Give the extent of all Plasmodium vivax-infected red blood cells.
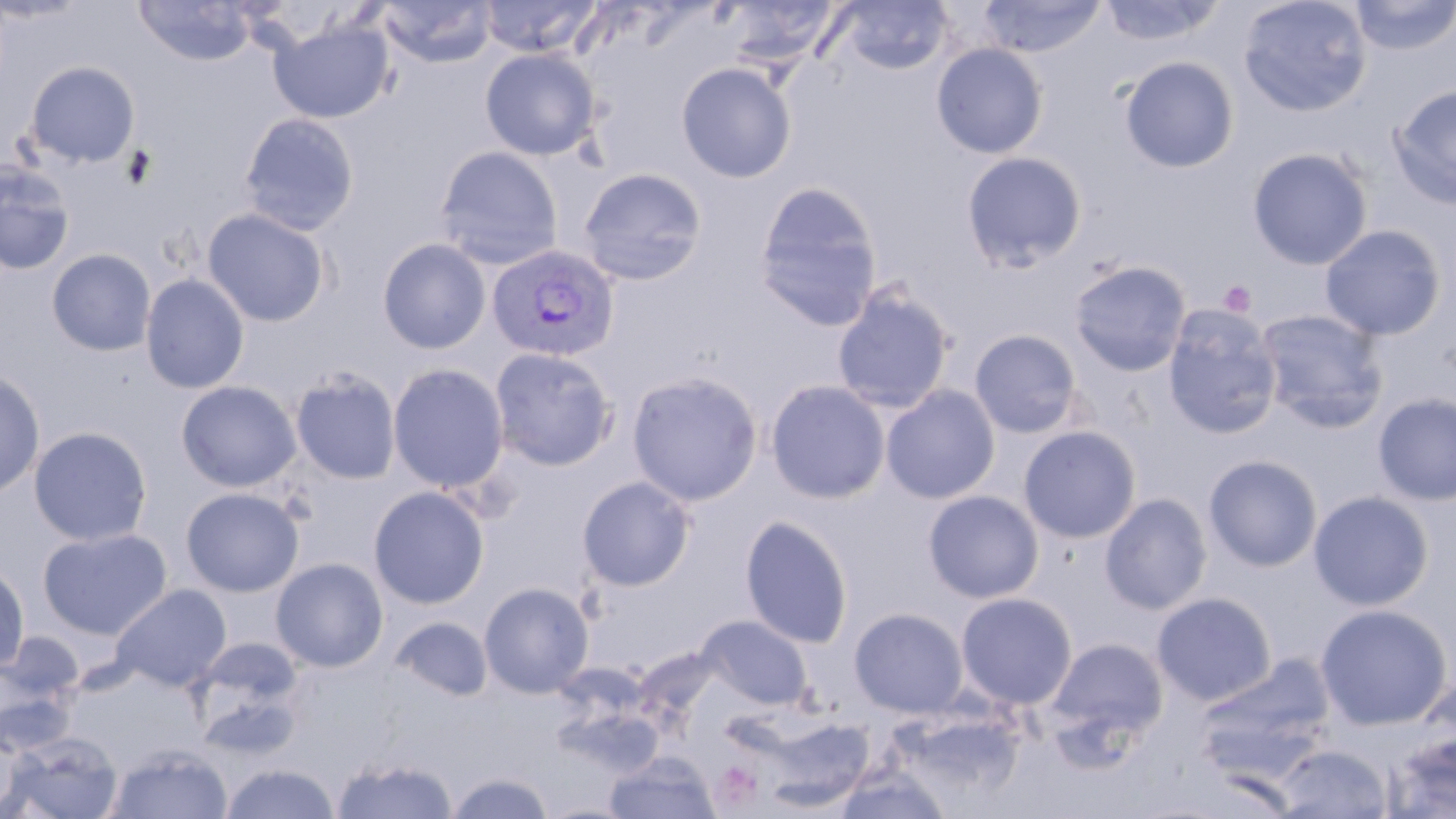

Approximate bounding boxes as [x1, y1, x2, y2] in pixels.
Plasmodium vivax-infected red blood cells: [487, 244, 621, 363].

Platelet locations: [1219, 280, 1256, 317], [713, 763, 761, 808]. Uninfected red blood cell locations: [133, 0, 258, 67], [378, 0, 497, 67], [478, 0, 601, 58], [720, 0, 842, 69], [834, 0, 953, 75], [977, 0, 1107, 58], [1098, 0, 1225, 46], [1238, 0, 1372, 117], [1349, 0, 1456, 55], [270, 20, 394, 123], [932, 43, 1048, 159], [480, 47, 602, 160], [1119, 56, 1239, 173], [24, 61, 140, 168], [676, 62, 796, 182], [1388, 84, 1456, 210], [240, 113, 359, 235], [435, 146, 563, 269], [1247, 147, 1372, 270], [961, 151, 1087, 272], [0, 160, 75, 275], [578, 167, 707, 286], [753, 181, 883, 332], [201, 207, 331, 327], [1319, 224, 1446, 341], [377, 238, 491, 354], [47, 248, 156, 356], [1070, 260, 1191, 377], [139, 273, 250, 394], [831, 285, 955, 413], [1163, 306, 1282, 439], [1255, 309, 1390, 434], [969, 329, 1082, 438], [489, 347, 619, 472], [388, 363, 509, 493], [289, 368, 402, 486], [0, 369, 45, 498], [626, 370, 763, 506], [766, 379, 891, 504], [175, 380, 302, 492], [881, 385, 1000, 504], [1372, 393, 1456, 506], [1018, 425, 1141, 544], [28, 426, 153, 546], [1203, 455, 1323, 572], [576, 475, 695, 592], [369, 486, 489, 609], [180, 487, 305, 597], [923, 490, 1044, 603], [936, 490, 1062, 708], [1308, 490, 1434, 611], [1100, 493, 1212, 614], [739, 515, 853, 649], [38, 528, 173, 640], [270, 557, 389, 673], [0, 562, 29, 672], [479, 581, 594, 698], [111, 584, 231, 691], [955, 591, 1077, 710], [1152, 592, 1276, 706], [1314, 604, 1452, 730], [849, 607, 969, 718], [696, 615, 813, 709], [391, 616, 493, 701], [189, 636, 307, 740], [1046, 637, 1168, 747], [0, 639, 82, 745], [1200, 656, 1336, 762], [758, 714, 876, 812], [0, 730, 37, 816], [4, 731, 123, 819], [1386, 732, 1456, 817], [1274, 743, 1392, 818], [105, 745, 233, 819], [606, 751, 717, 819], [332, 754, 457, 819], [220, 762, 340, 819], [831, 766, 953, 818], [446, 771, 555, 817]. Slide-level diagnosis: Plasmodium vivax. Single field of view. Thin blood smear. May-Grünwald-Giemsa-stained preparation. 1000x magnification. Image is 1456×819 pixels. Optical microscopy.